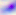 400x magnification. Micrograph. Toxoplasma gondii is shown.